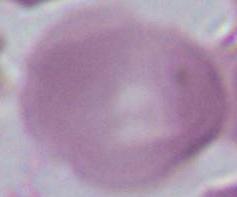

magnification = 1000x
modality = micrograph
identification = erythrocyte